Locate every Plasmodium falciparum-infected red blood cell.
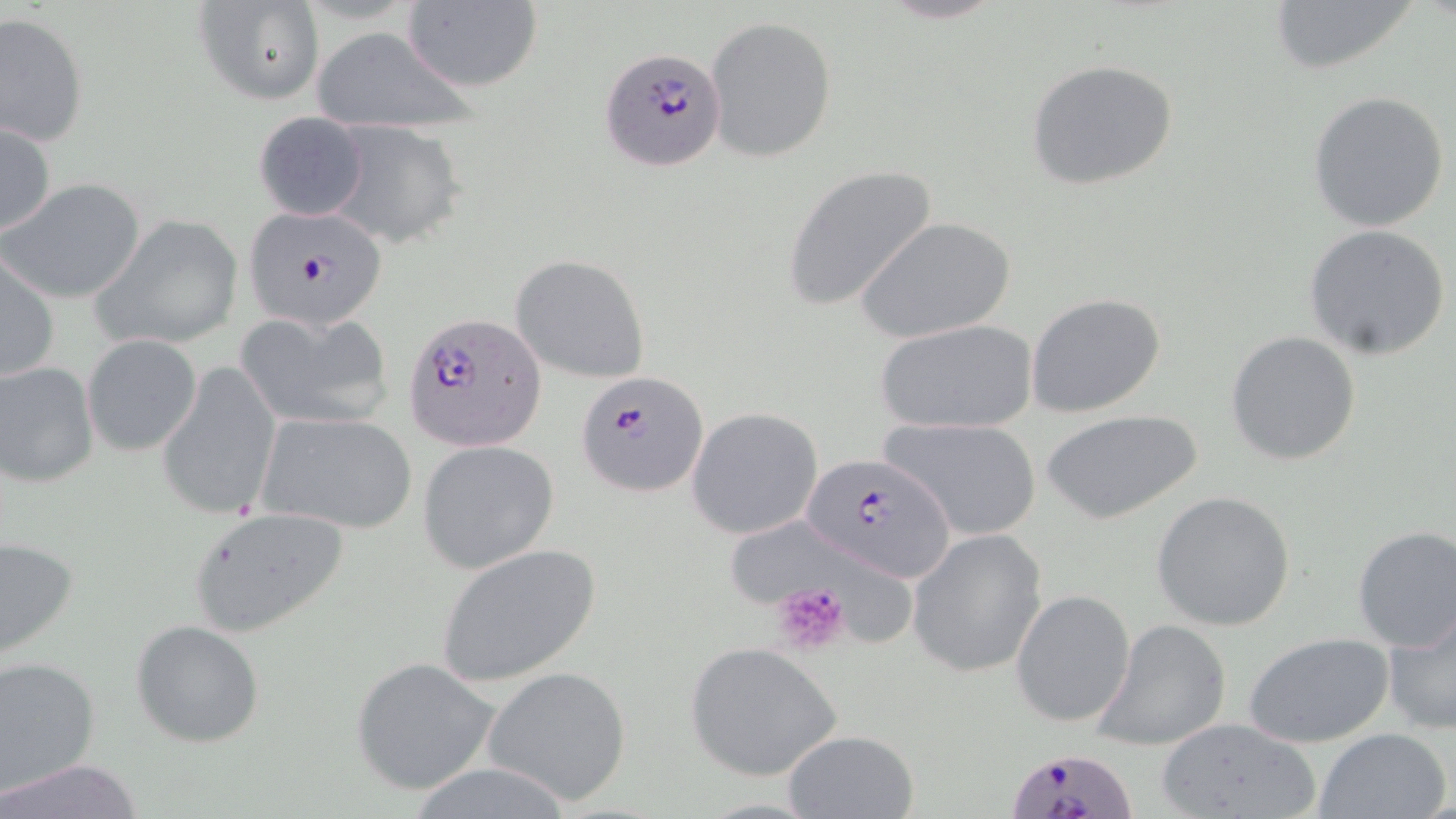

Approximate bounding boxes as (x1, y1, x2, y2) in pixels.
Plasmodium falciparum-infected red blood cells: (599, 47, 726, 171), (242, 210, 389, 329), (404, 312, 545, 452), (578, 370, 708, 498), (803, 449, 959, 579), (1007, 743, 1136, 818).

Summary:
  - Uninfected red blood cell locations: (1263, 0, 1426, 76), (192, 2, 324, 107), (399, 2, 542, 95), (1, 12, 89, 146), (705, 15, 837, 163), (311, 27, 469, 133), (1025, 58, 1179, 191), (1307, 90, 1450, 232), (251, 110, 371, 221), (0, 120, 56, 239), (321, 120, 466, 248), (780, 165, 939, 313), (3, 178, 146, 304), (91, 214, 245, 350), (856, 217, 1015, 343), (1303, 224, 1451, 362), (1, 252, 60, 385), (509, 254, 650, 384), (1025, 292, 1167, 417), (235, 308, 397, 431), (874, 318, 1039, 435), (1226, 330, 1363, 467), (83, 333, 202, 456), (0, 360, 99, 489), (156, 362, 284, 520), (686, 407, 823, 540), (1041, 408, 1205, 525), (254, 410, 418, 536), (880, 415, 1044, 543), (418, 440, 560, 576), (1151, 491, 1296, 631), (189, 506, 348, 636), (731, 523, 918, 649), (1352, 527, 1456, 651), (908, 529, 1047, 678), (0, 535, 79, 663), (436, 543, 602, 688), (1010, 589, 1136, 728), (1382, 609, 1456, 737), (1091, 619, 1234, 751), (131, 620, 265, 748), (1246, 633, 1393, 748), (685, 641, 846, 781), (0, 654, 101, 799), (352, 656, 501, 795), (484, 667, 633, 803), (1155, 716, 1321, 819), (1312, 728, 1451, 819), (781, 729, 918, 818), (0, 760, 147, 818)
  - Platelet locations: (769, 581, 852, 655)
  - Slide-level diagnosis: Plasmodium falciparum
  - Preparation: thin blood film
  - Magnification: 1000x
  - Field of view: single
  - Modality: light microscopy
  - Stain: May-Grünwald-Giemsa
  - Image size: 1456×819 pixels